Report the malaria status of this cell.
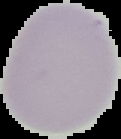

Uninfected.

Segmented cell region on a black background. From a thin blood smear. Image is 121×139 pixels.